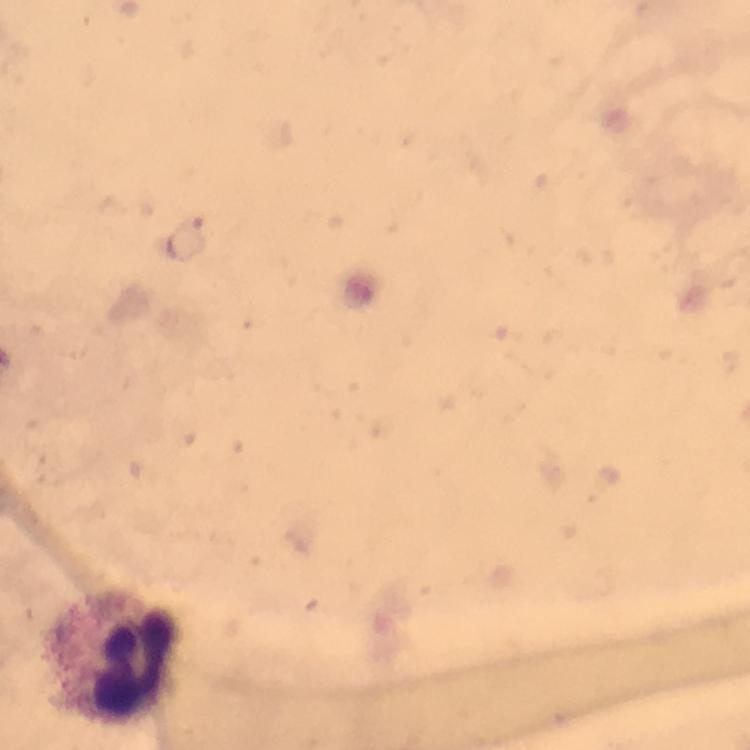

{
  "cropped_from": "a single field of view",
  "preparation": "thick blood smear",
  "capture": "smartphone mounted on the microscope",
  "leukocyte_locations": "approximate centers as (x, y) in pixels: (120, 656)",
  "magnification": "100x",
  "context": "from a diagnostic examination for malaria",
  "image_size": "750×750 pixels",
  "plasmodium_parasite_locations": "approximate centers as (x, y) in pixels: (190, 240)",
  "stain": "Giemsa",
  "immersion_oil": "used"
}